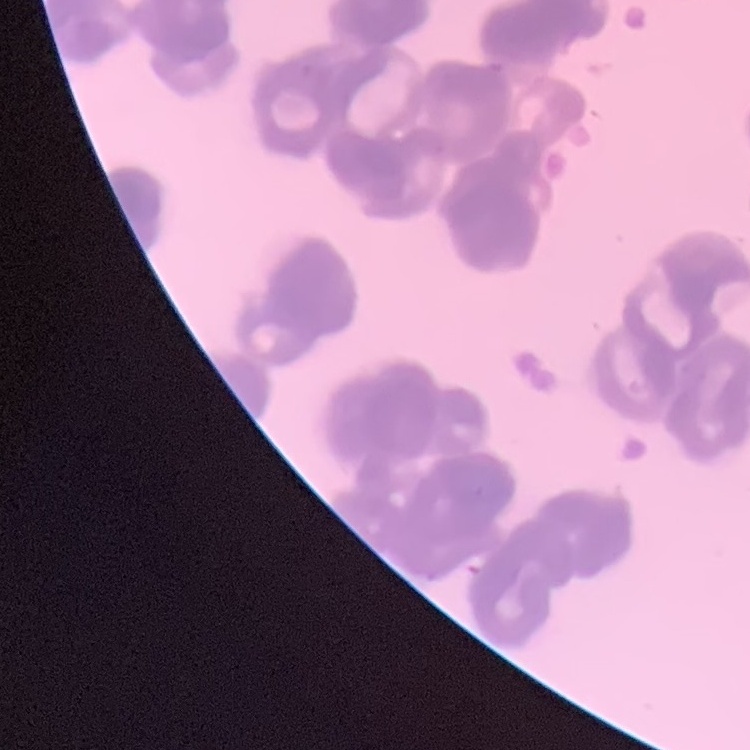
{
  "red_blood_cell_morphology": "rouleaux formation",
  "preparation": "thin blood film",
  "stain": "Field's or Giemsa",
  "image_type": "square crop of a larger photomicrograph"
}